Describe the morphology of the erythrocytes.
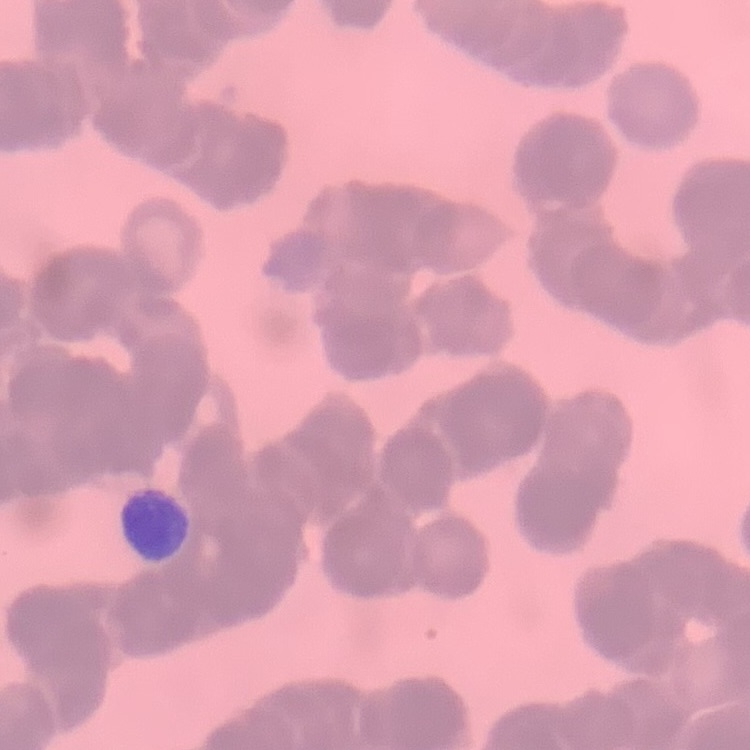
Rouleaux formation.

{
  "preparation": "thin peripheral smear",
  "stain": "Field's or Giemsa",
  "image_type": "square crop of a larger photomicrograph"
}